Report the malaria status of this cell.
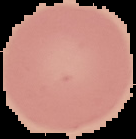

Uninfected.

Summary:
  - Image type: segmented cell region on a black background
  - Preparation: thin blood film
  - Image size: 136×139 pixels